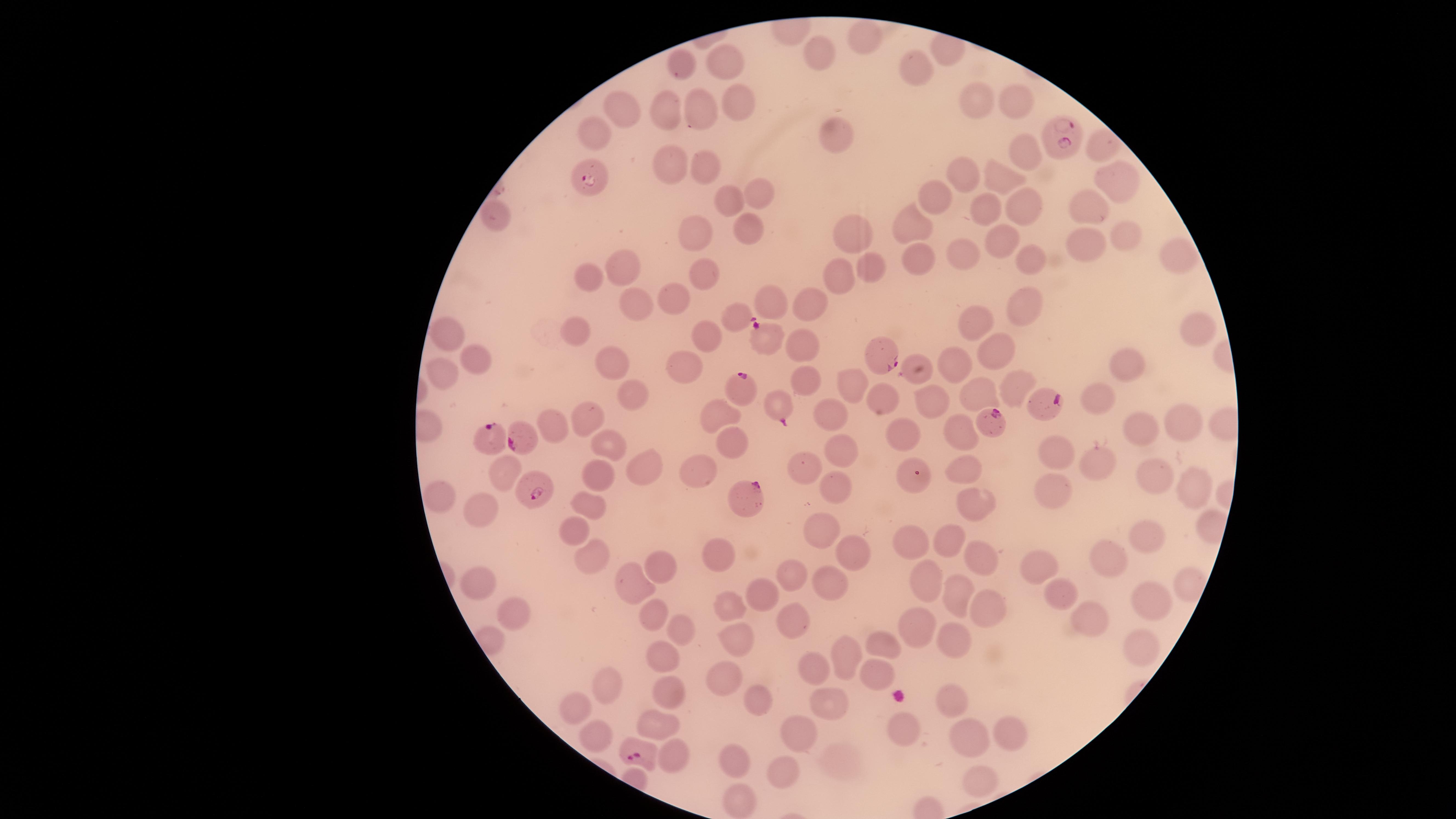
Approximate marker points as [x, y] in pixels.
Summary:
  - Uninfected red blood cells: [869, 39], [816, 55], [680, 61], [721, 64], [921, 67], [1016, 95], [736, 102], [978, 105], [666, 107], [699, 110], [624, 111], [841, 131], [596, 133], [1100, 143], [1020, 152], [668, 163], [704, 164], [958, 172], [999, 173], [1115, 181], [759, 194], [929, 197], [729, 199], [1023, 203], [1088, 203], [988, 209], [493, 213], [919, 224], [750, 225], [851, 229], [694, 230], [1129, 238], [998, 241], [1080, 243], [962, 251], [1171, 253], [915, 258], [1026, 258], [621, 267], [870, 269], [591, 272], [840, 274], [699, 275], [674, 298], [772, 301], [805, 302], [1023, 304], [647, 309], [976, 327], [577, 329], [1199, 329], [446, 332], [708, 333], [804, 340], [992, 349], [475, 356], [613, 358], [958, 363], [1125, 366], [684, 368], [444, 371], [803, 380], [847, 380], [1015, 382], [974, 389], [637, 394], [931, 400], [1101, 403], [716, 410], [836, 416], [587, 417], [552, 421], [1188, 423], [895, 428], [1143, 428], [965, 432], [609, 443], [730, 444], [840, 447], [1055, 451], [1097, 461], [802, 463], [968, 464], [643, 466], [502, 470], [700, 474], [597, 475], [1150, 477], [838, 484], [1196, 484], [1059, 490], [441, 494], [973, 500], [477, 505], [585, 506], [817, 529], [570, 531], [1144, 532], [951, 540], [912, 541], [724, 553], [850, 554], [975, 556], [589, 557], [1111, 557], [1040, 562], [656, 566], [794, 574], [927, 581], [631, 582], [478, 583], [1191, 583], [757, 585], [831, 588], [958, 595], [1068, 595], [1150, 606], [725, 607], [988, 609], [510, 612], [785, 616], [651, 617], [1083, 622], [924, 626], [676, 631], [737, 637], [960, 641], [884, 643], [1137, 647], [844, 655], [662, 660], [811, 668], [874, 674], [721, 677], [607, 685], [750, 691], [671, 693], [956, 703], [830, 704], [568, 706], [658, 726], [906, 730], [1010, 730], [596, 733], [805, 735], [963, 736], [672, 754], [736, 762], [787, 772], [978, 779], [739, 801]
  - Parasitized red blood cells: [1064, 136], [589, 179], [735, 312], [765, 336], [885, 350], [742, 389], [780, 405], [1048, 405], [993, 423], [521, 439], [494, 440], [920, 476], [745, 492], [538, 493], [637, 752]
  - Capture: smartphone photograph through the microscope eyepiece
  - Presence: malaria parasites seen
  - Species: Plasmodium falciparum
  - Stain: Giemsa
  - Preparation: thin blood smear
  - Field of view: single
  - Visible region: circular
  - Image size: 1456×819 pixels